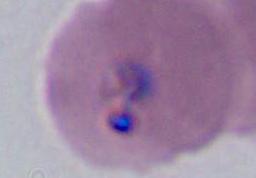 Micrograph. A Plasmodium parasite is seen. 400x or 1000x magnification.